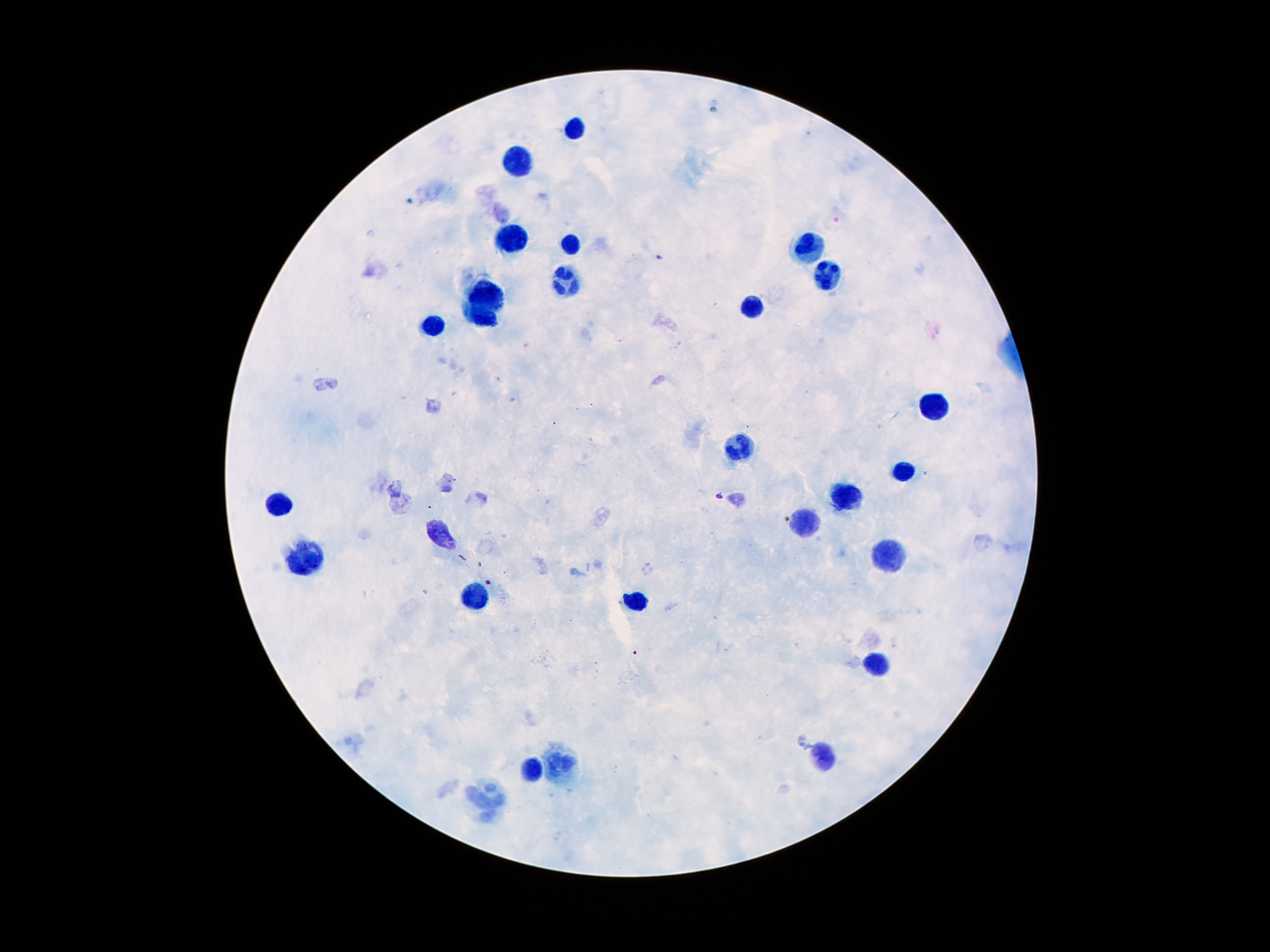

Approximate centers as [x, y] in pixels.
Summary:
  - Leukocyte locations: [576, 127], [518, 167], [510, 242], [807, 245], [569, 246], [825, 279], [567, 283], [490, 300], [752, 311], [482, 317], [435, 328], [932, 406], [739, 448], [901, 470], [844, 495], [278, 503], [806, 521], [441, 534], [891, 559], [303, 562], [472, 596], [635, 601], [876, 665], [823, 755], [559, 766], [532, 768], [489, 801]
  - Plasmodium parasite locations: [658, 257], [717, 497]
  - Patient malaria status: infected with Plasmodium falciparum
  - Image size: 1270×952 pixels
  - Field of view: single
  - Stain: Giemsa
  - Capture: smartphone camera through the microscope eyepiece
  - Magnification: 100x
  - Preparation: thick peripheral-blood smear